Name the cell type shown.
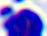

A leukocyte.

magnification = 400x
modality = micrograph